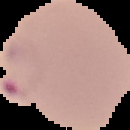

Summary:
  - Preparation: thin blood smear
  - Image size: 130×130 pixels
  - Image type: segmented cell region on a black background
  - Result: malaria parasites detected